Point out each leukocyte.
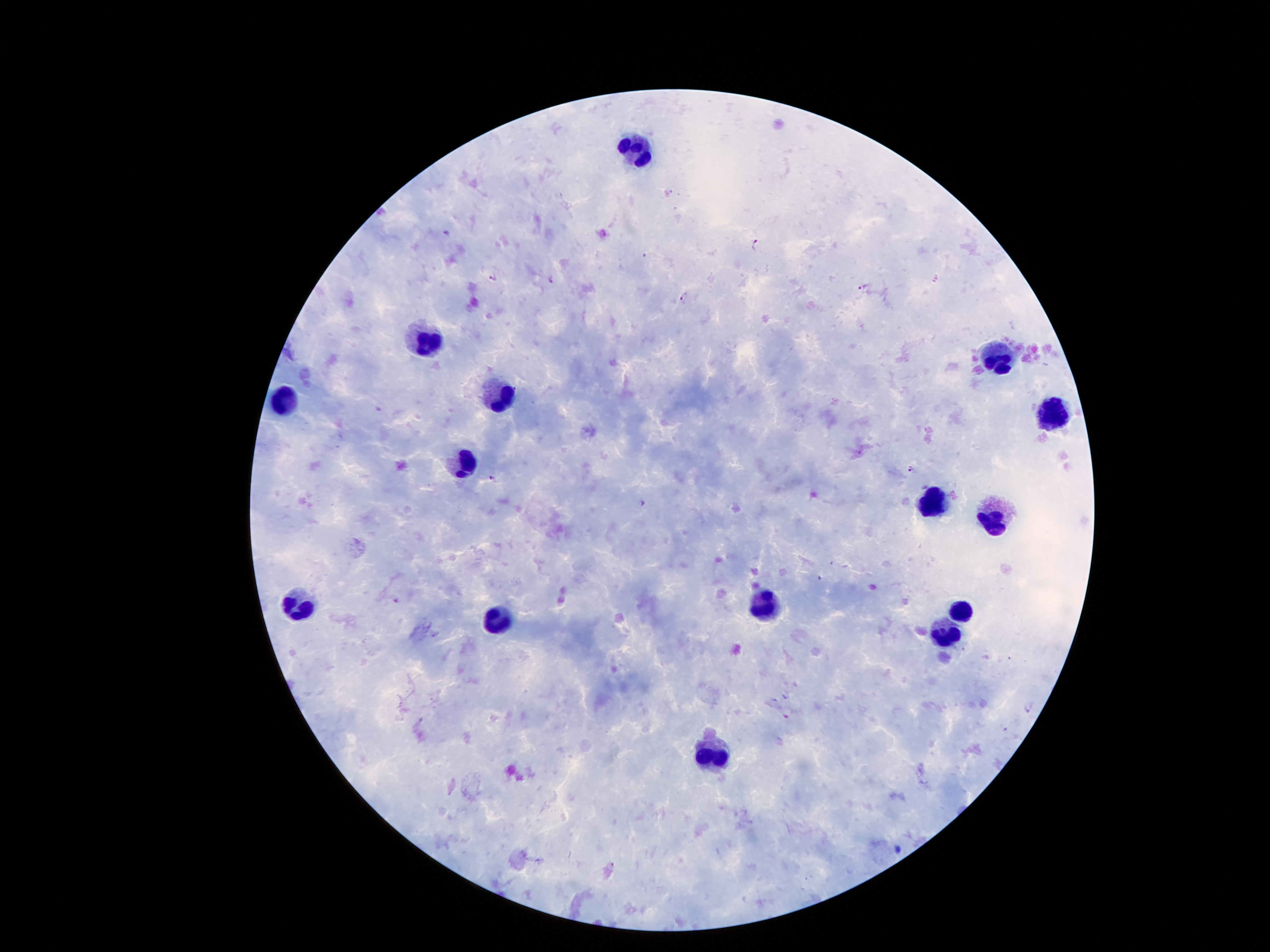

Approximate object centers, in pixels from the top-left corner.
Leukocytes: (x=632, y=149), (x=430, y=338), (x=996, y=356), (x=500, y=399), (x=281, y=401), (x=1049, y=416), (x=461, y=467), (x=930, y=503), (x=992, y=513), (x=298, y=600), (x=764, y=607), (x=963, y=609), (x=495, y=619), (x=948, y=636), (x=711, y=753).

malaria parasite locations = (x=445, y=231), (x=756, y=243), (x=644, y=256), (x=495, y=277), (x=550, y=281), (x=864, y=286), (x=685, y=296), (x=912, y=471), (x=490, y=478), (x=642, y=504), (x=399, y=599), (x=786, y=696), (x=776, y=701), (x=786, y=714), (x=900, y=848)
field of view = single
patient malaria status = infected with Plasmodium falciparum
image size = 1270×952 pixels
capture = smartphone through the microscope eyepiece
preparation = thick blood film
stain = Giemsa
magnification = 100x